Describe the morphology of the red blood cells.
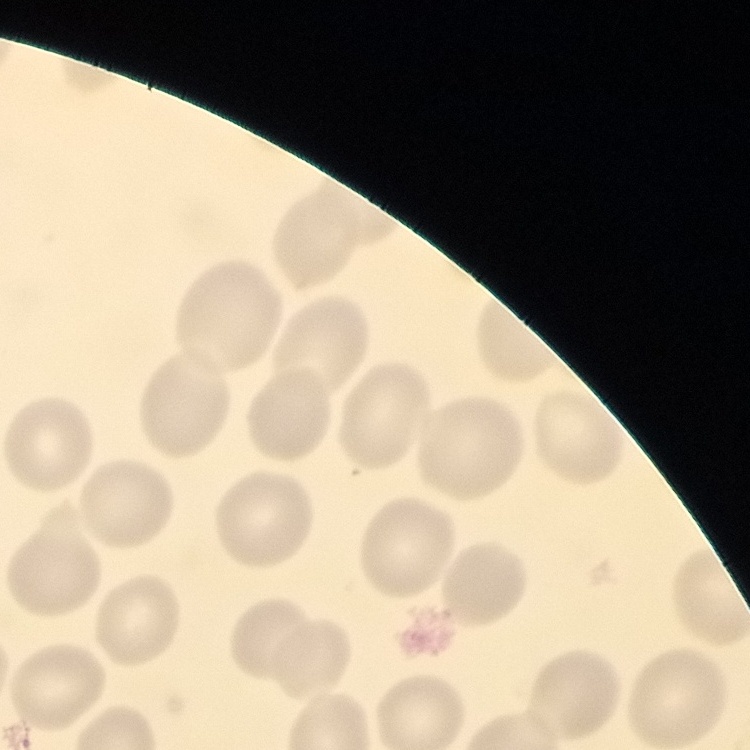
They show no rouleaux formation.

{
  "image_type": "one tile cut from a larger photomicrograph",
  "preparation": "thin blood smear",
  "stain": "Field's or Giemsa"
}